Locate every blood parasite and identify its species.
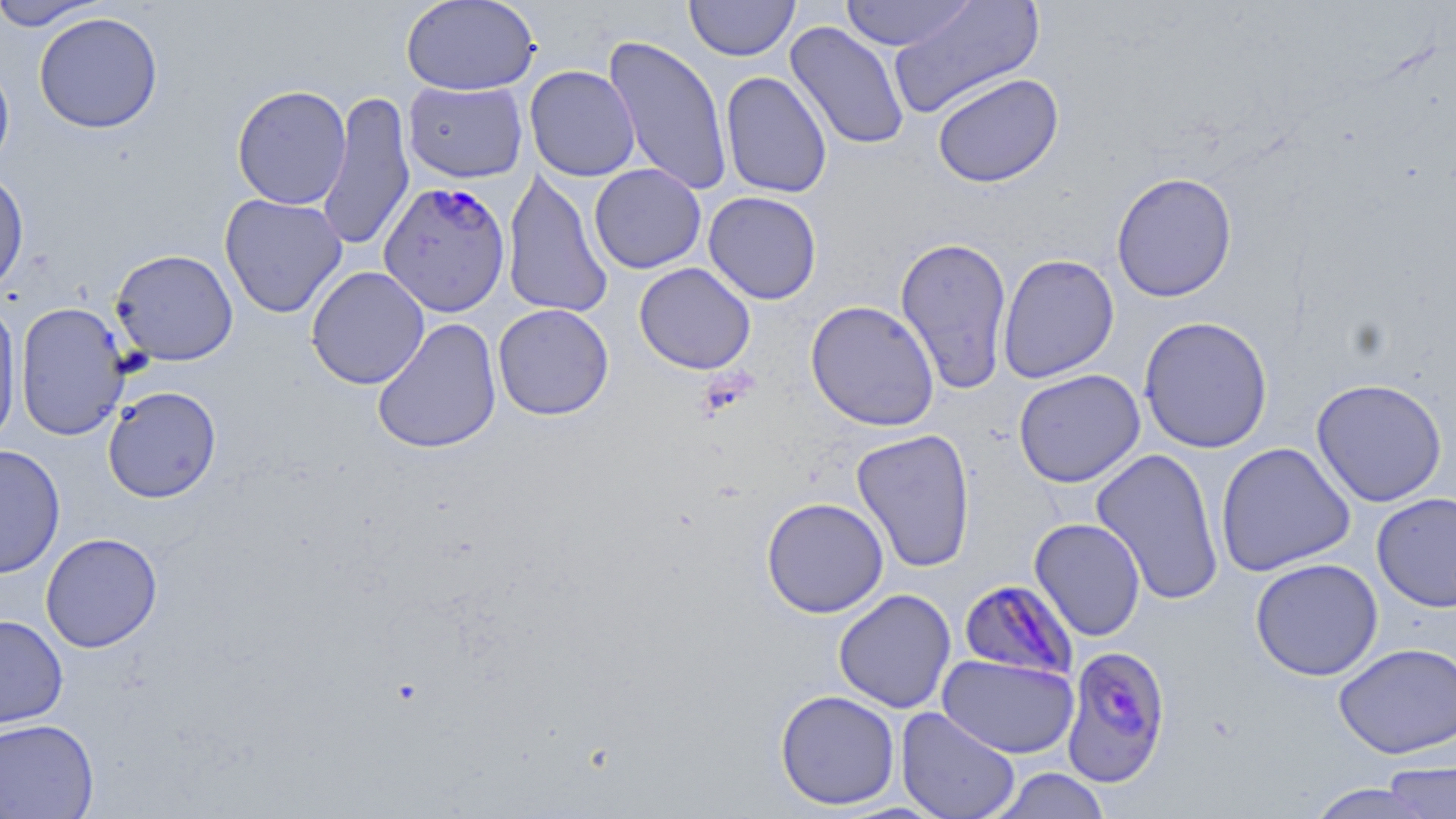

Approximate bounding boxes as (x1,y1)-(x2,y2) corner pairs in pixels.
Plasmodium falciparum-infected red blood cells: (378,180)-(511,317), (959,577)-(1078,681), (1061,643)-(1173,786).
No Plasmodium ovale, Plasmodium malariae, Plasmodium vivax, Babesia divergens, or Trypanosoma brucei observed.

Summary:
  - Uninfected red blood cell locations: (0,0)-(109,30), (401,0)-(540,96), (839,0)-(979,51), (685,1)-(799,61), (887,1)-(1045,120), (33,12)-(163,134), (785,21)-(910,151), (603,35)-(734,197), (0,57)-(15,177), (524,65)-(640,182), (720,71)-(832,199), (932,72)-(1064,188), (402,80)-(528,183), (231,84)-(352,210), (318,90)-(416,253), (589,163)-(706,274), (501,167)-(614,319), (0,169)-(29,298), (1111,172)-(1238,302), (703,191)-(822,305), (220,193)-(347,318), (895,235)-(1013,394), (110,249)-(239,365), (997,253)-(1120,383), (634,262)-(756,374), (305,266)-(430,389), (805,300)-(940,431), (0,301)-(22,446), (14,301)-(130,441), (493,303)-(614,420), (1138,315)-(1273,454), (372,318)-(501,454), (1013,369)-(1145,488), (1311,378)-(1448,507), (102,386)-(222,503), (851,428)-(976,573), (1215,442)-(1355,577), (0,444)-(66,579), (1090,447)-(1225,605), (1372,492)-(1456,613), (761,497)-(889,618), (1029,518)-(1146,641), (40,533)-(162,653), (1250,558)-(1384,681), (833,588)-(957,713), (0,614)-(68,730), (1333,641)-(1456,759), (937,654)-(1079,759), (775,689)-(900,810), (895,706)-(1021,819), (0,717)-(99,819), (1383,757)-(1455,817), (987,767)-(1112,819), (1303,782)-(1441,819)
  - Slide-level diagnosis: Plasmodium falciparum
  - Preparation: thin blood smear
  - Magnification: 1000x
  - Field of view: one of a larger specimen
  - Modality: optical microscopy
  - Stain: May-Grünwald-Giemsa
  - Image size: 1456×819 pixels